Locate and identify every blood parasite.
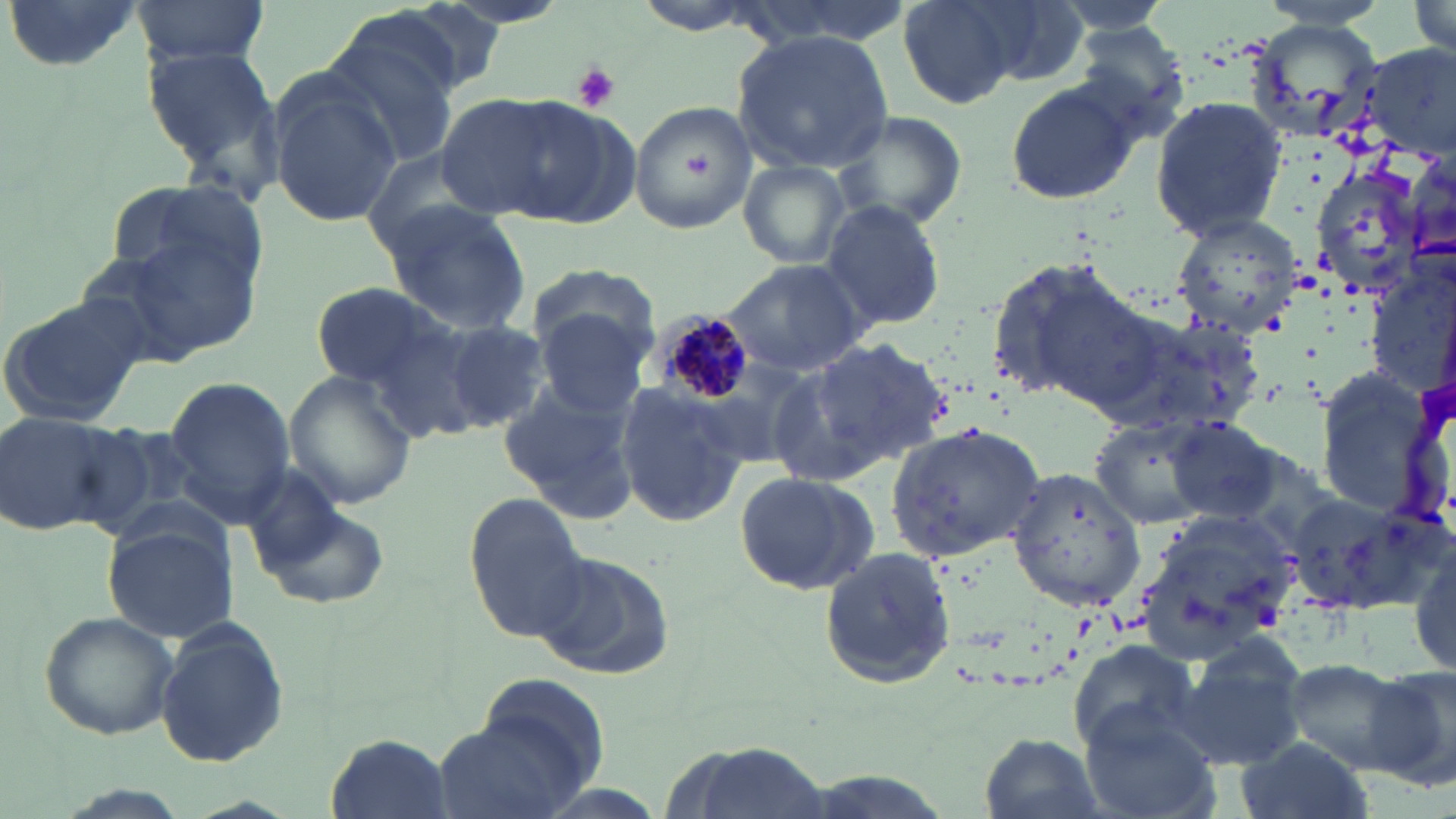
Approximate bounding boxes as named x1/y1/x2/y2 corners in pixels.
Plasmodium malariae-infected red blood cells: (x1=647, y1=306, x2=759, y2=404).
No Plasmodium falciparum, Plasmodium ovale, Plasmodium vivax, Babesia divergens, or Trypanosoma brucei observed.

Summary:
  - Uninfected red blood cell locations: (x1=1, y1=0, x2=146, y2=74), (x1=134, y1=0, x2=270, y2=67), (x1=901, y1=0, x2=1023, y2=107), (x1=962, y1=0, x2=1092, y2=90), (x1=319, y1=19, x2=464, y2=168), (x1=1071, y1=22, x2=1192, y2=142), (x1=732, y1=31, x2=893, y2=175), (x1=141, y1=38, x2=287, y2=188), (x1=267, y1=72, x2=401, y2=226), (x1=1004, y1=80, x2=1143, y2=206), (x1=437, y1=92, x2=604, y2=220), (x1=1150, y1=94, x2=1287, y2=238), (x1=630, y1=98, x2=758, y2=231), (x1=834, y1=108, x2=968, y2=231), (x1=736, y1=160, x2=851, y2=272), (x1=1306, y1=160, x2=1432, y2=296), (x1=106, y1=181, x2=270, y2=295), (x1=818, y1=196, x2=947, y2=331), (x1=381, y1=201, x2=531, y2=332), (x1=1170, y1=213, x2=1305, y2=334), (x1=88, y1=230, x2=262, y2=366), (x1=982, y1=254, x2=1154, y2=414), (x1=721, y1=259, x2=870, y2=379), (x1=1364, y1=263, x2=1456, y2=401), (x1=310, y1=283, x2=449, y2=388), (x1=527, y1=290, x2=658, y2=418), (x1=1, y1=291, x2=150, y2=428), (x1=1091, y1=308, x2=1267, y2=442), (x1=440, y1=322, x2=549, y2=432), (x1=810, y1=335, x2=954, y2=467), (x1=761, y1=361, x2=892, y2=486), (x1=1313, y1=366, x2=1433, y2=513), (x1=286, y1=372, x2=416, y2=512), (x1=162, y1=375, x2=297, y2=517), (x1=500, y1=381, x2=639, y2=518), (x1=614, y1=381, x2=747, y2=531), (x1=0, y1=409, x2=132, y2=538), (x1=1085, y1=415, x2=1223, y2=532), (x1=1165, y1=416, x2=1285, y2=525), (x1=883, y1=423, x2=1049, y2=562), (x1=1006, y1=465, x2=1146, y2=614), (x1=733, y1=469, x2=878, y2=596), (x1=1279, y1=485, x2=1432, y2=621), (x1=255, y1=497, x2=389, y2=609), (x1=464, y1=497, x2=592, y2=642), (x1=1134, y1=510, x2=1293, y2=661), (x1=103, y1=521, x2=239, y2=643), (x1=817, y1=546, x2=957, y2=692), (x1=532, y1=548, x2=675, y2=681), (x1=1413, y1=558, x2=1454, y2=672), (x1=39, y1=611, x2=180, y2=741), (x1=154, y1=618, x2=292, y2=768), (x1=1065, y1=639, x2=1199, y2=758), (x1=1173, y1=641, x2=1311, y2=770), (x1=1279, y1=657, x2=1418, y2=767), (x1=1363, y1=662, x2=1456, y2=792), (x1=441, y1=689, x2=604, y2=819), (x1=1078, y1=709, x2=1222, y2=819), (x1=328, y1=732, x2=450, y2=817), (x1=977, y1=733, x2=1107, y2=819), (x1=1232, y1=737, x2=1371, y2=819), (x1=663, y1=739, x2=832, y2=819)
  - Platelet locations: (x1=569, y1=63, x2=621, y2=112)
  - Slide-level diagnosis: Plasmodium malariae
  - Stain: May-Grünwald-Giemsa
  - Modality: light microscopy
  - Magnification: 1000x
  - Image size: 1456×819 pixels
  - Field of view: single
  - Preparation: thin blood film